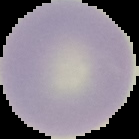

image size = 139×139 pixels
result = no Plasmodium parasites detected
preparation = thin blood film
image type = segmented cell region on a black background